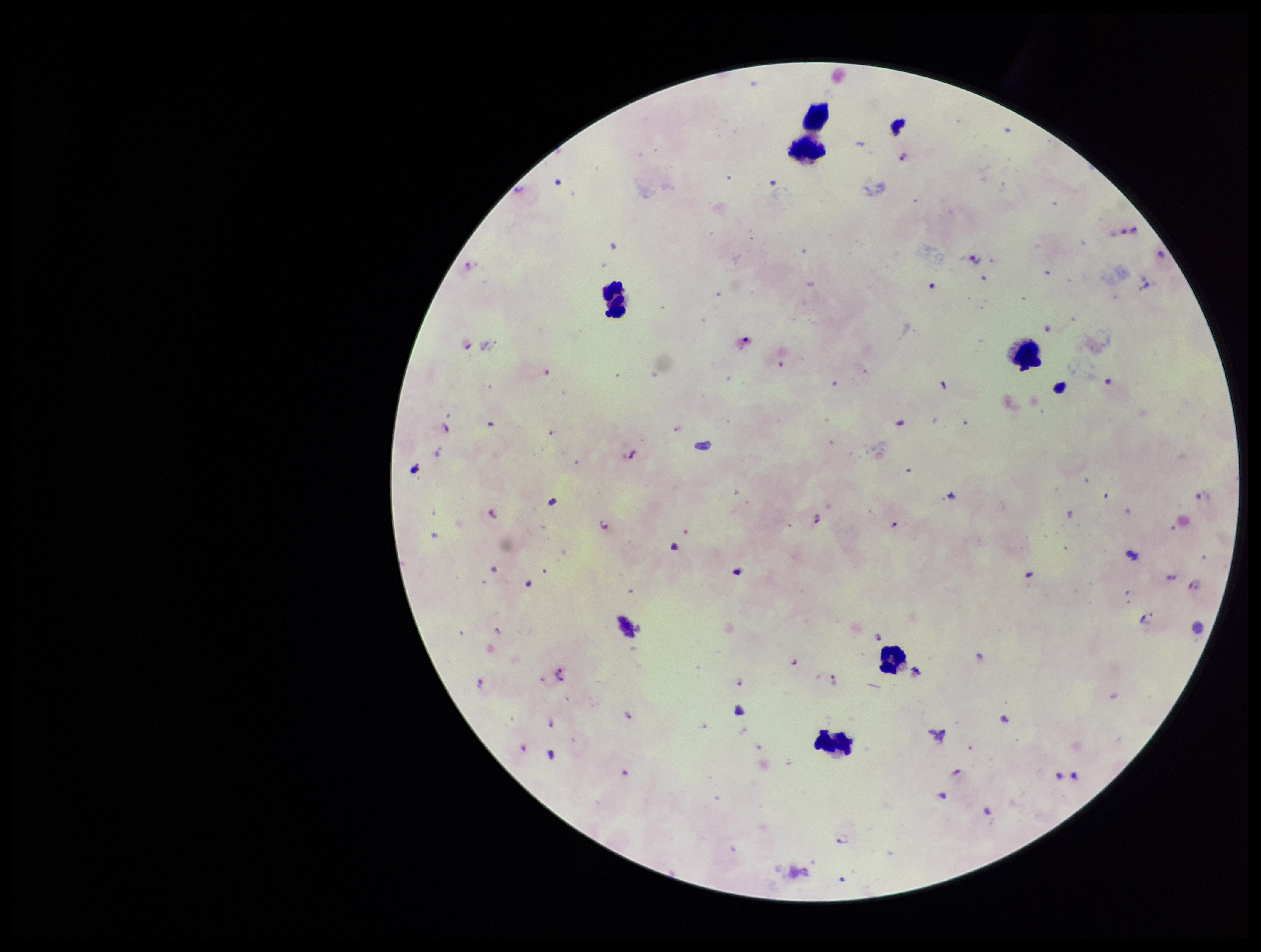
patient malaria status = positive
capture = smartphone photograph through the microscope eyepiece
Plasmodium parasites = identified
leukocyte count = 6
preparation = thick blood smear
field of view = single
species reported for this patient = Plasmodium falciparum
parasite count = 14
image size = 1261×952 pixels
stain = Giemsa